Comment on the morphology of the erythrocytes.
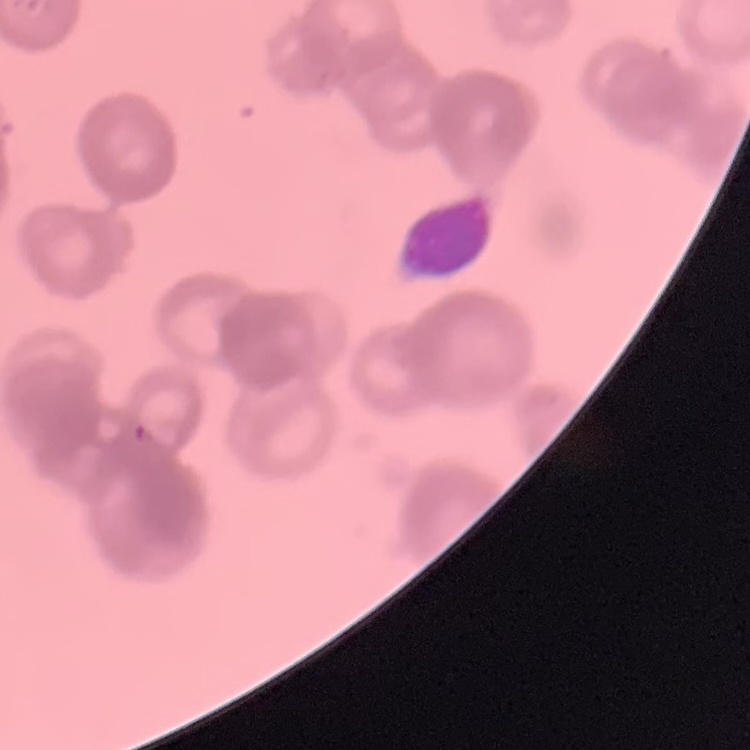

They show rouleaux formation.

Square crop of a larger photomicrograph. Thin peripheral smear. Field's or Giemsa stain.